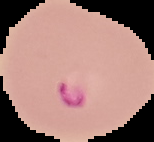

{
  "result": "malaria parasites identified",
  "image_type": "segmented cell region on a black background",
  "preparation": "thin blood film",
  "image_size": "154×142 pixels"
}